Classify this cell by malaria status.
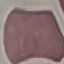
Uninfected.

Summary:
  - Stain: Giemsa
  - Preparation: thin blood film
  - Image type: automatically extracted cell patch, resized to 64 × 64 pixels
  - Capture: smartphone through the microscope eyepiece